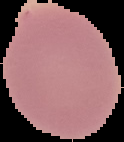
image_size: 124×142 pixels
malaria_status: uninfected
preparation: thin blood film
image_type: segmented cell region with the area outside set to black